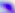

magnification = 400x
modality = photomicrograph
identification = Toxoplasma gondii